Give the extent of all uninfected red blood cells.
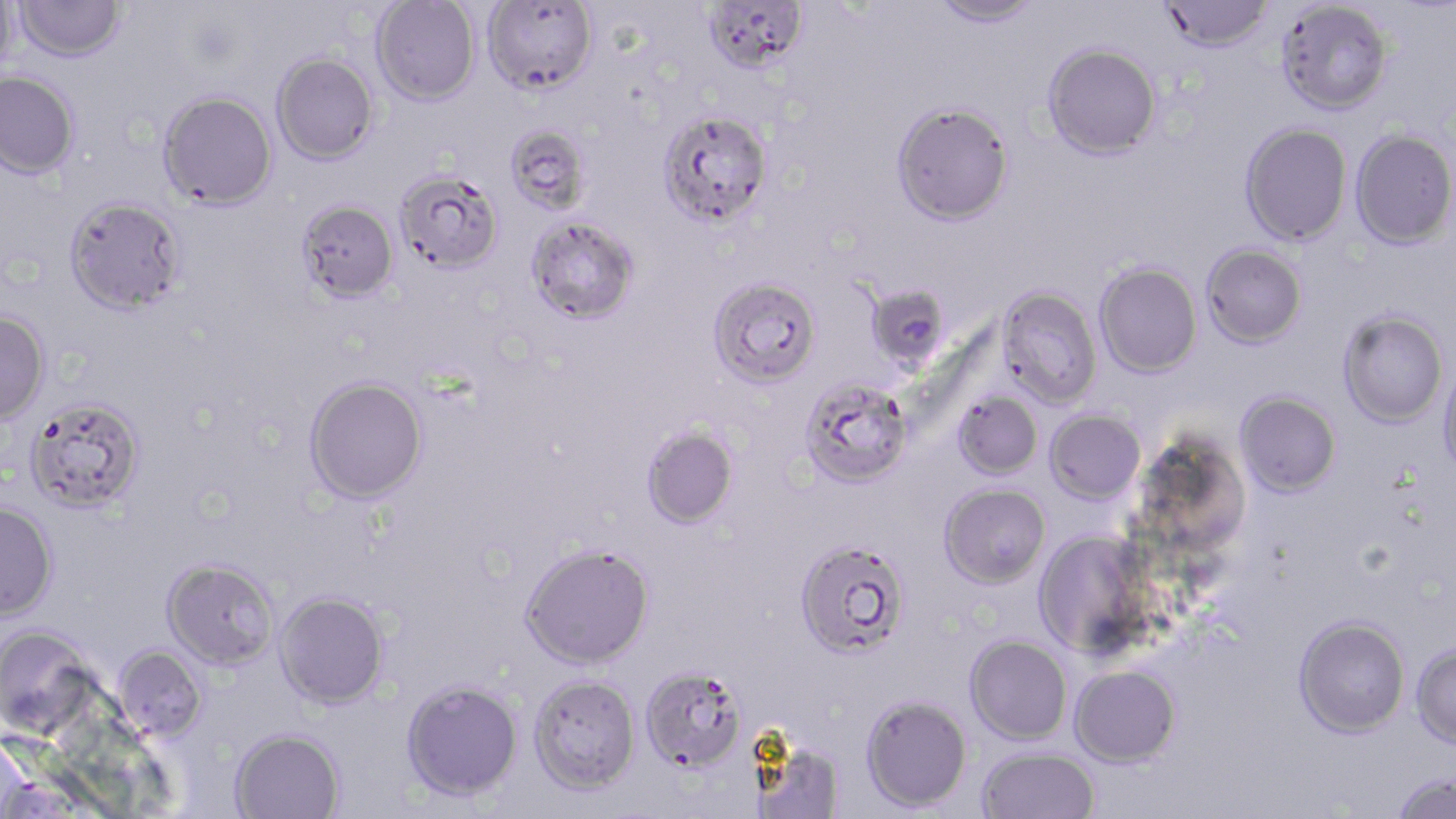

Approximate bounding boxes as (x1,y1)-(x2,y2) corner pairs in pixels.
Uninfected red blood cells: (0,0)-(19,76), (482,0)-(599,95), (700,0)-(809,74), (930,0)-(1043,28), (1160,0)-(1275,52), (14,1)-(126,62), (370,1)-(481,106), (1276,1)-(1392,114), (1042,42)-(1162,160), (272,52)-(378,164), (0,71)-(80,179), (157,90)-(277,209), (891,100)-(1014,225), (657,108)-(773,227), (1240,122)-(1352,246), (504,124)-(593,215), (1350,129)-(1456,249), (394,169)-(505,275), (63,196)-(187,315), (296,199)-(399,303), (525,216)-(640,325), (1201,243)-(1307,348), (1094,262)-(1203,378), (708,277)-(821,388), (870,285)-(949,376), (996,287)-(1103,408), (1338,310)-(1448,428), (0,311)-(50,424), (1437,363)-(1456,482), (304,376)-(428,505), (799,378)-(913,488), (953,391)-(1043,480), (1234,391)-(1341,497), (25,397)-(145,514), (1045,410)-(1146,505), (641,425)-(738,529), (939,483)-(1051,589), (0,501)-(59,622), (1033,531)-(1151,658), (795,539)-(910,659), (520,543)-(655,669), (162,558)-(280,670), (274,590)-(390,709), (1293,615)-(1410,738), (0,625)-(99,738), (965,635)-(1072,744), (1410,642)-(1456,750), (112,645)-(208,742), (639,664)-(748,773), (1069,665)-(1180,768), (529,673)-(640,794), (401,679)-(523,801), (859,694)-(971,811), (230,728)-(345,819), (750,737)-(846,819), (977,747)-(1099,819), (1391,772)-(1456,819).

Summary:
  - Slide-level diagnosis: Plasmodium falciparum
  - Stain: May-Grünwald-Giemsa
  - Modality: optical microscopy
  - Field of view: single
  - Preparation: thin blood film
  - Magnification: 1000x
  - Image size: 1456×819 pixels